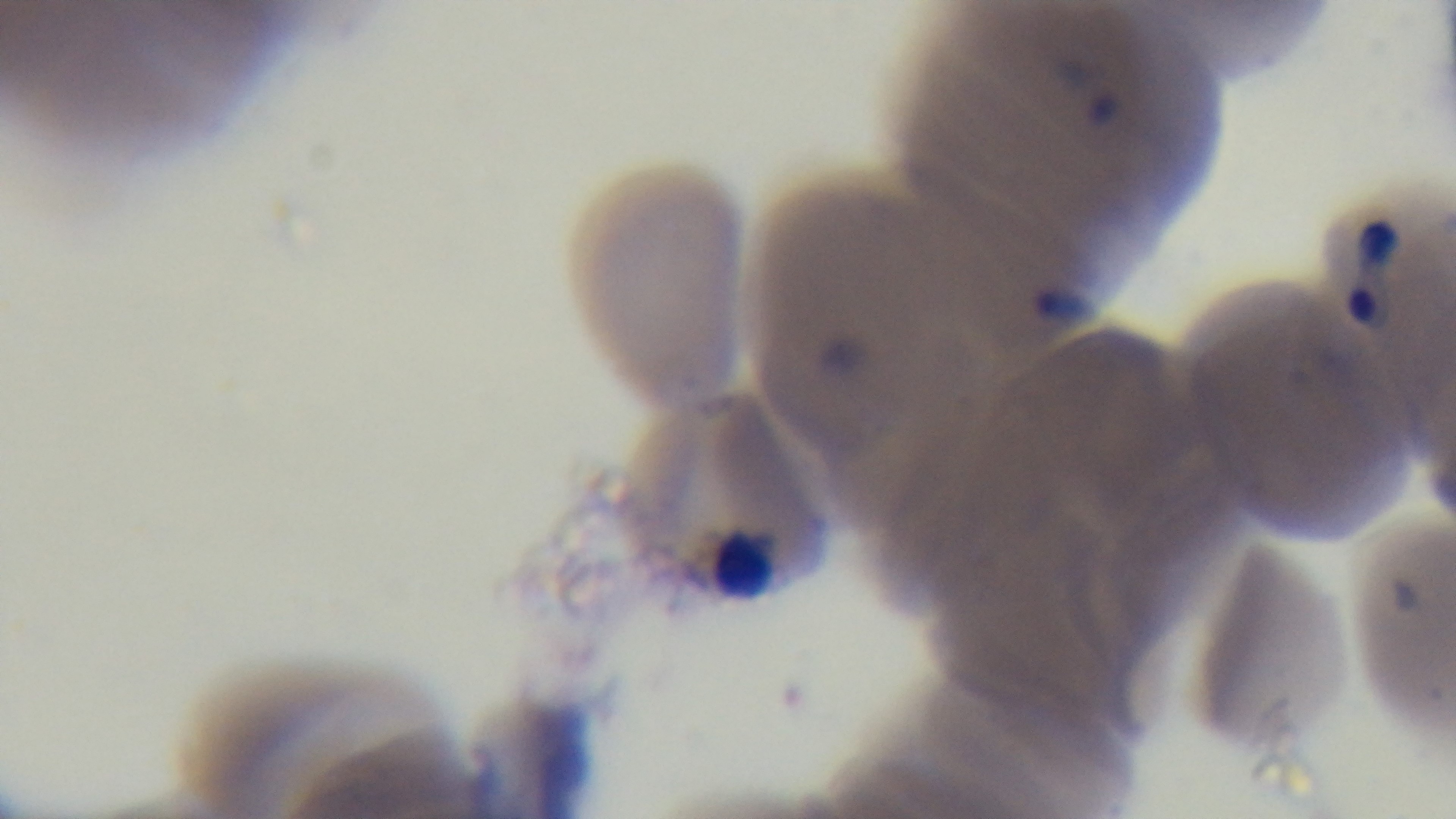

field of view = one from the slide
objective = 100x oil immersion
stain = Giemsa
malaria status = infected
preparation = thin
capture = mounted 4K digital camera
modality = light microscopy